Locate every Plasmodium parasite.
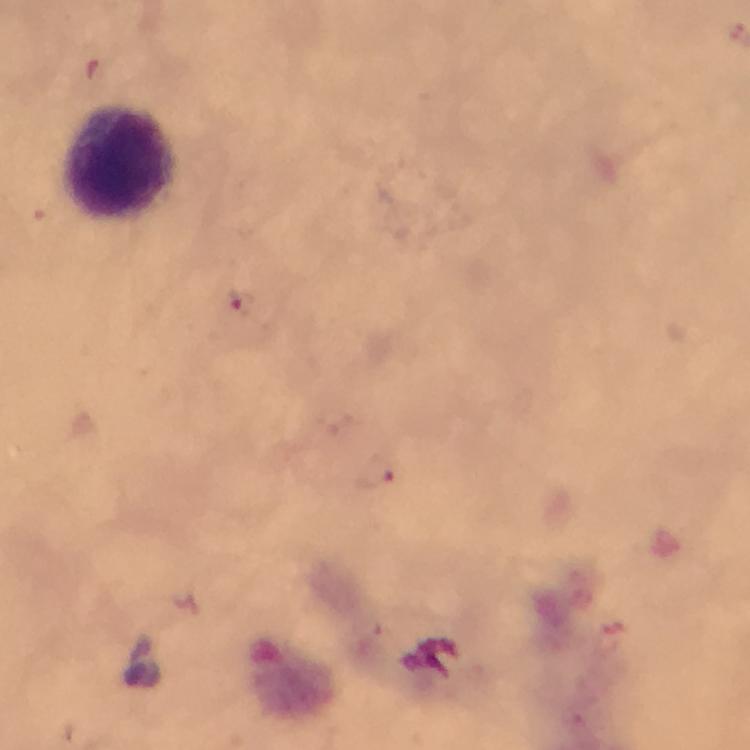
Approximate centers as (x, y) in pixels.
Plasmodium parasites: (241, 303), (375, 473).

stain = Giemsa
capture = smartphone photograph through a microscope
immersion oil = used
context = from a malaria diagnostic workup
magnification = 100x
leukocyte locations = approximate centers as (x, y) in pixels: (125, 164)
image size = 750×750 pixels
cropped from = a single field of view
preparation = thick blood smear